Locate every Plasmodium parasite.
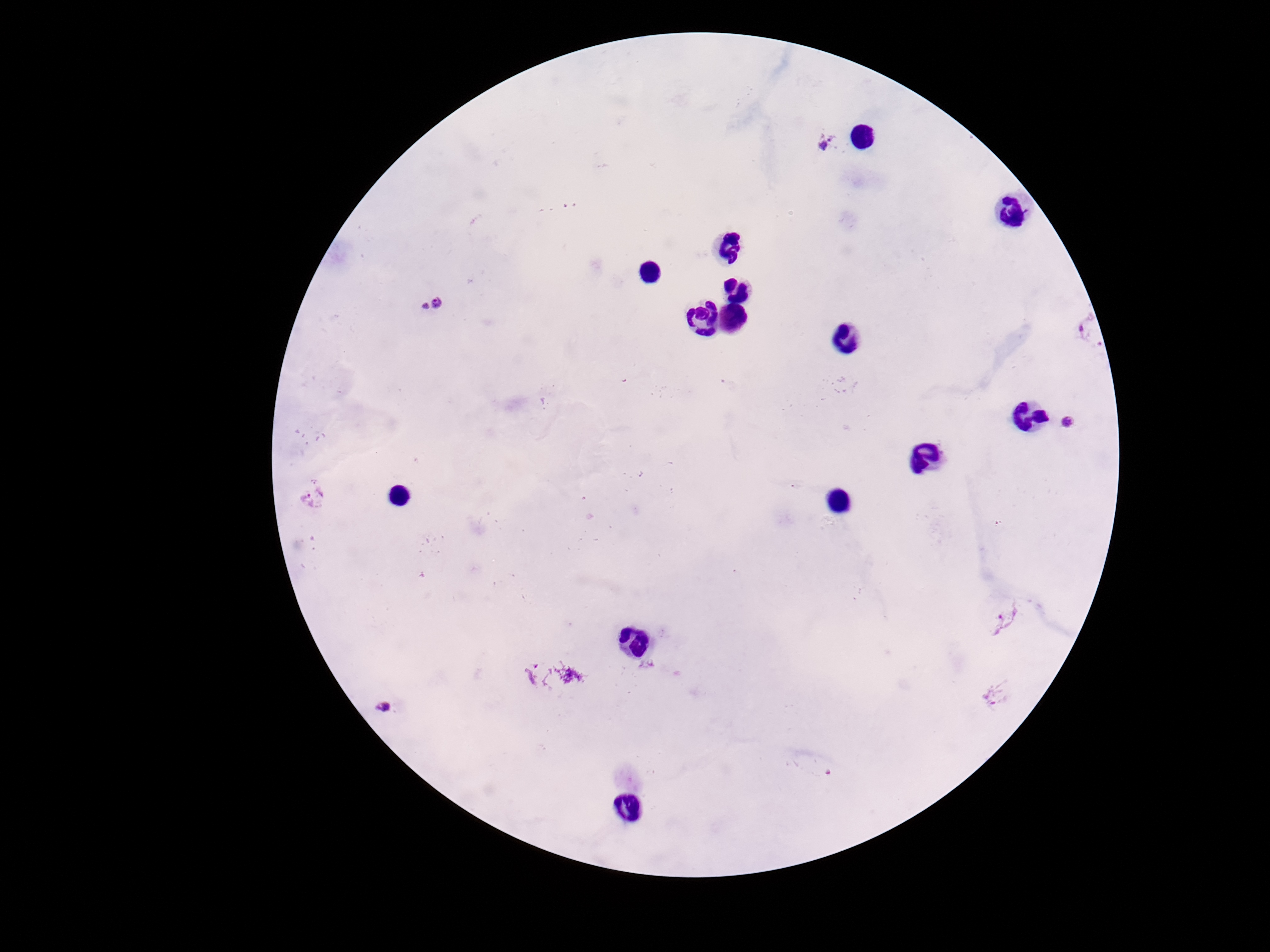
Approximate centers as [x, y] in pixels.
Plasmodium parasites: [832, 143], [433, 307], [1074, 330], [1073, 422], [314, 498], [1008, 619], [995, 696], [386, 706].

Summary:
  - Patient malaria status: positive
  - Stain: Giemsa
  - Preparation: thick blood smear
  - Image size: 1270×952 pixels
  - Magnification: 100x
  - Field of view: single
  - Capture: smartphone camera through the microscope eyepiece